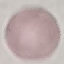
result = negative for malaria parasites
capture = smartphone camera at the microscope eyepiece
stain = Giemsa
image type = cell patch, automatically extracted from a larger field of view and resized to 64 × 64 pixels
preparation = thin blood smear